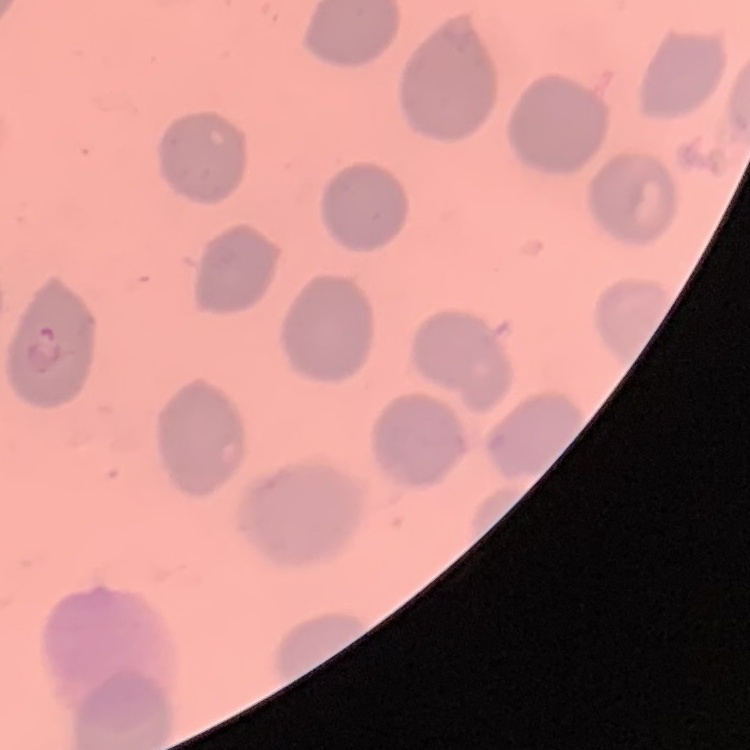

red blood cell morphology = no rouleaux formation
preparation = thin blood film
image type = one tile cut from a larger photomicrograph
stain = Field's or Giemsa